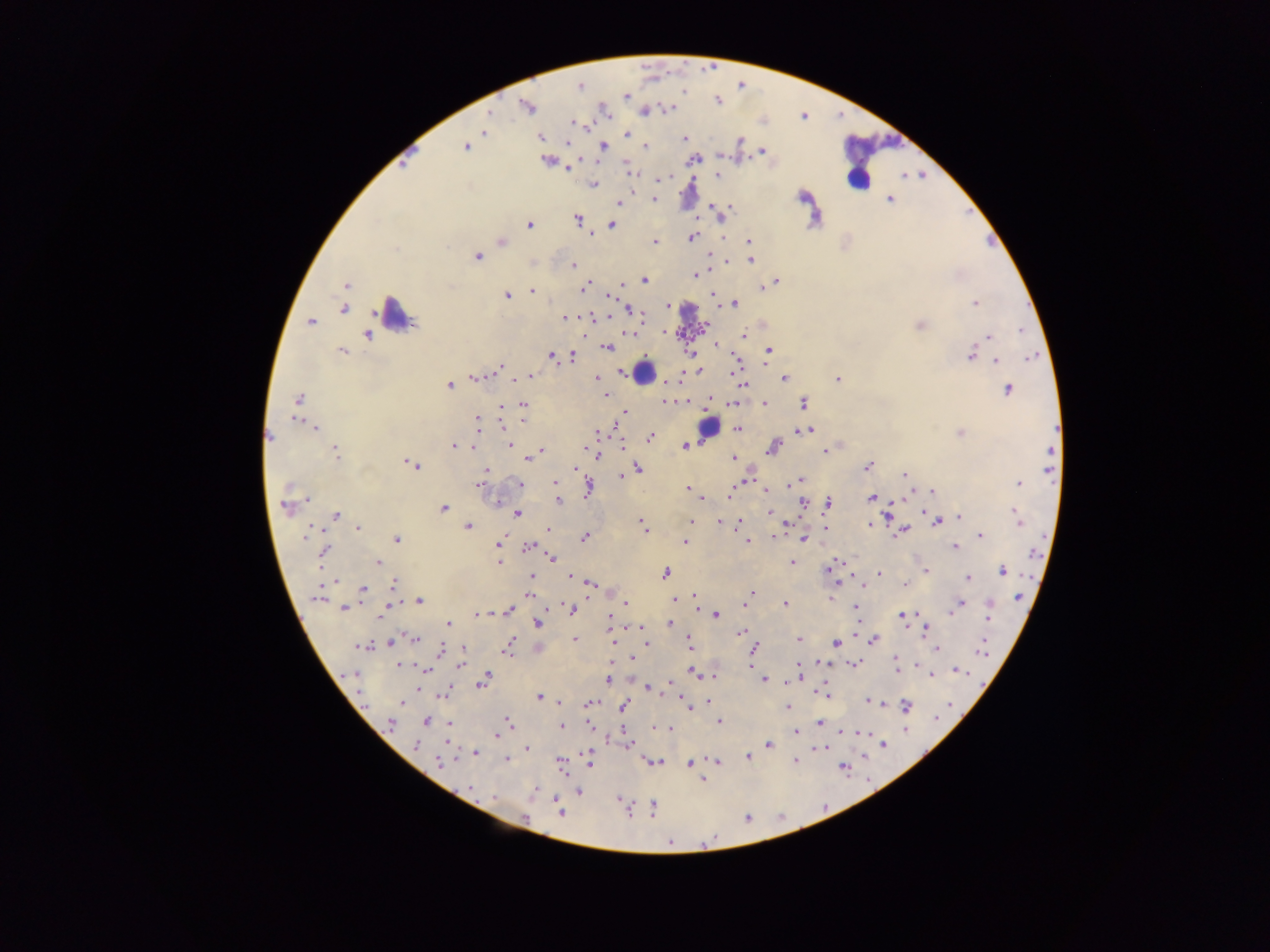
Approximate centers as (x, y) in pixels. Malaria parasite locations: (713, 69), (580, 85), (625, 96), (718, 100), (527, 107), (668, 108), (644, 111), (487, 115), (804, 122), (574, 123), (483, 132), (627, 134), (540, 137), (683, 139), (567, 141), (739, 141), (465, 146), (603, 146), (646, 147), (408, 149), (762, 151), (545, 159), (693, 159), (568, 169), (628, 171), (717, 174), (664, 176), (900, 176), (659, 179), (592, 184), (803, 196), (889, 199), (654, 200), (617, 202), (710, 204), (970, 214), (577, 220), (529, 224), (611, 224), (590, 233), (692, 237), (748, 240), (986, 240), (655, 241), (502, 242), (477, 256), (710, 257), (750, 259), (573, 265), (695, 274), (644, 280), (775, 281), (622, 282), (346, 285), (767, 285), (583, 287), (761, 288), (531, 290), (712, 294), (507, 295), (609, 297), (734, 303), (974, 303), (668, 305), (343, 308), (629, 309), (565, 317), (590, 317), (311, 322), (920, 325), (704, 327), (664, 331), (368, 334), (628, 334), (743, 336), (988, 336), (715, 344), (607, 347), (342, 350), (768, 350), (975, 350), (690, 352), (971, 354), (551, 355), (571, 357), (995, 360), (736, 365), (499, 366), (697, 370), (528, 376), (473, 377), (597, 377), (783, 378), (837, 378), (679, 380), (448, 385), (742, 385), (1007, 389), (605, 395), (297, 399), (709, 400), (663, 401), (685, 401), (523, 403), (733, 403), (804, 403), (763, 404), (502, 408), (623, 411), (523, 420), (478, 421), (615, 425), (314, 427), (738, 429), (798, 430), (807, 430), (598, 432), (960, 432), (269, 436), (650, 437), (687, 444), (511, 445), (622, 445), (454, 446), (472, 447), (773, 447), (584, 448), (830, 449), (334, 450), (541, 450), (824, 450), (597, 454), (528, 456), (734, 457), (412, 464), (869, 466), (577, 468), (638, 468), (486, 470), (904, 474), (621, 477), (799, 479), (554, 482), (1018, 484), (519, 485), (792, 485), (479, 486), (687, 487), (587, 488), (765, 489), (729, 490), (933, 491), (872, 497), (702, 498), (558, 500), (803, 501), (495, 502), (826, 504), (443, 507), (286, 508), (1013, 510), (769, 512), (517, 513), (335, 515), (886, 516), (959, 518), (937, 521), (1018, 521), (691, 522), (718, 522), (738, 523), (641, 524), (869, 525), (467, 526), (823, 527), (357, 528), (549, 529), (644, 529), (903, 530), (772, 535), (980, 535), (584, 537), (397, 538), (803, 538), (685, 542), (747, 542), (498, 543), (528, 546), (954, 546), (323, 552), (499, 556), (551, 558), (377, 562), (498, 562), (791, 562), (829, 567), (924, 570), (1002, 571), (665, 573), (879, 573), (569, 574), (533, 576), (967, 578), (531, 580), (332, 581), (837, 582), (589, 583), (394, 584), (905, 584), (859, 585), (362, 590), (750, 592), (531, 595), (1017, 596), (317, 597), (829, 598), (694, 599), (418, 600), (675, 600), (625, 602), (744, 604), (784, 604), (959, 604), (698, 605), (989, 605), (345, 607), (855, 607), (387, 608), (572, 609), (508, 610), (949, 613), (477, 614), (716, 614), (609, 615), (902, 616), (988, 617), (670, 623), (856, 623), (448, 624), (538, 624), (633, 627), (925, 630), (743, 632), (413, 639), (688, 639), (574, 640), (798, 640), (873, 640), (392, 641), (613, 641), (647, 644), (836, 644), (983, 644), (363, 646), (508, 646), (540, 646), (937, 648), (462, 649), (440, 651), (754, 651), (752, 657), (895, 659), (631, 661), (855, 662), (798, 663), (820, 663), (916, 664), (400, 665), (459, 665), (751, 668), (425, 669), (897, 669), (956, 670), (692, 671), (930, 676), (712, 677), (764, 679), (607, 680), (482, 681), (787, 682), (669, 683), (418, 686), (647, 688), (444, 693), (827, 695), (539, 696), (400, 701), (868, 701), (560, 702), (710, 702), (589, 704), (624, 704), (905, 706), (688, 708), (788, 708), (941, 712), (425, 721), (719, 721), (507, 722), (390, 723), (819, 723), (449, 724), (559, 725), (589, 725), (655, 726), (665, 728), (671, 728), (841, 731), (796, 732), (864, 733), (497, 734), (414, 744), (627, 744), (884, 744), (769, 745), (817, 746), (822, 747), (526, 748), (475, 753), (589, 755), (747, 756), (862, 756), (507, 759), (441, 760), (795, 760), (653, 761), (717, 761), (589, 762), (561, 763), (690, 764), (844, 771), (703, 780), (534, 788), (471, 789), (578, 791), (493, 796), (618, 799), (823, 805), (653, 808), (628, 810), (559, 811), (779, 813), (748, 815), (525, 819), (666, 831), (714, 838). Leukocyte locations: (869, 157), (859, 170), (857, 179), (396, 315), (644, 372), (709, 428). Mobile-phone photograph taken through the microscope. Image is 1270×952 pixels. Sample from Ghana. Thick blood film. Single field of view.